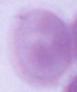
magnification = 1000x
identification = erythrocyte
modality = micrograph